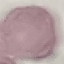
malaria status = uninfected
preparation = thin blood film
capture = smartphone camera at the microscope eyepiece
stain = Giemsa
image type = automatically extracted cell patch, resized to 64 × 64 pixels